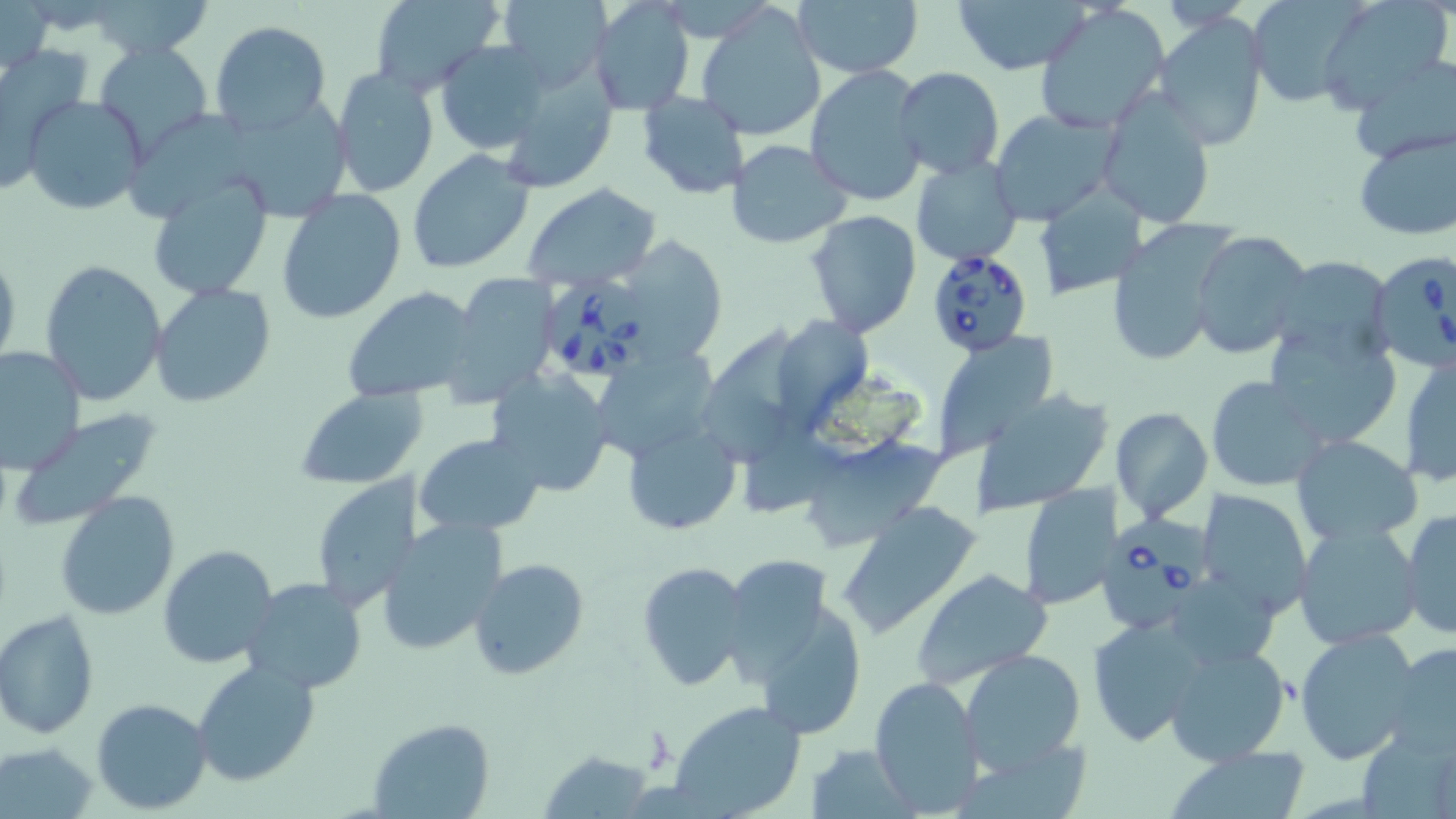 Approximate bounding boxes as (x1, y1, x2, y2) in pixels. Uninfected red blood cell locations: (88, 0, 216, 62), (498, 0, 610, 90), (589, 0, 695, 116), (792, 0, 923, 79), (951, 0, 1095, 74), (1247, 0, 1360, 106), (1318, 0, 1454, 112), (0, 1, 52, 81), (367, 1, 506, 98), (695, 3, 826, 140), (1035, 5, 1169, 134), (1156, 15, 1269, 151), (209, 20, 332, 136), (435, 39, 551, 156), (94, 43, 213, 157), (0, 45, 94, 175), (1352, 55, 1455, 162), (498, 64, 619, 193), (803, 66, 926, 207), (331, 67, 440, 197), (895, 68, 1005, 180), (637, 91, 751, 199), (1098, 91, 1217, 228), (240, 92, 362, 216), (23, 94, 148, 216), (990, 108, 1119, 224), (131, 110, 255, 224), (1351, 127, 1456, 240), (726, 139, 852, 249), (406, 150, 535, 274), (912, 157, 1024, 267), (145, 173, 273, 300), (520, 182, 663, 291), (1036, 182, 1148, 299), (276, 188, 407, 323), (805, 210, 921, 337), (1102, 216, 1238, 368), (1191, 230, 1313, 360), (620, 236, 727, 365), (0, 247, 21, 377), (1269, 258, 1395, 350), (40, 260, 168, 406), (443, 274, 561, 405), (149, 284, 275, 407), (342, 287, 483, 406), (780, 312, 868, 432), (705, 318, 802, 468), (1262, 318, 1402, 449), (928, 330, 1060, 459), (0, 345, 84, 475), (594, 347, 719, 464), (1400, 353, 1456, 486), (486, 369, 616, 497), (1205, 375, 1328, 492), (295, 386, 427, 491), (976, 390, 1112, 514), (1111, 407, 1214, 524), (7, 411, 163, 532), (622, 423, 741, 536), (414, 432, 547, 536), (804, 434, 954, 546), (1290, 434, 1423, 546), (314, 476, 421, 613), (1017, 482, 1117, 608), (1195, 488, 1313, 618), (55, 490, 181, 621), (833, 502, 985, 638), (1400, 509, 1455, 639), (375, 516, 509, 656), (1292, 520, 1423, 650), (157, 543, 280, 669), (469, 559, 591, 681), (733, 559, 828, 691), (636, 562, 752, 692), (908, 567, 1055, 691), (242, 578, 369, 695), (754, 600, 870, 743), (0, 610, 98, 739), (1086, 612, 1211, 744), (1295, 626, 1422, 765), (1163, 640, 1292, 767), (1386, 641, 1456, 755), (960, 649, 1087, 772), (191, 661, 319, 788), (868, 675, 984, 815), (91, 698, 212, 814), (668, 699, 806, 819), (366, 718, 495, 819), (1358, 724, 1454, 819), (808, 741, 915, 816), (3, 742, 101, 815), (1165, 745, 1314, 819), (539, 749, 657, 817). Babesia divergens-infected red blood cell locations: (923, 246, 1031, 355), (1368, 248, 1456, 374), (549, 273, 646, 386), (1098, 510, 1210, 638). Slide-level diagnosis: Babesia divergens. Thin blood film. May-Grünwald-Giemsa stain. Light microscopy. Captured at 1000x magnification. Image is 1456×819 pixels. Single field of view.